Outline each uninfected red blood cell.
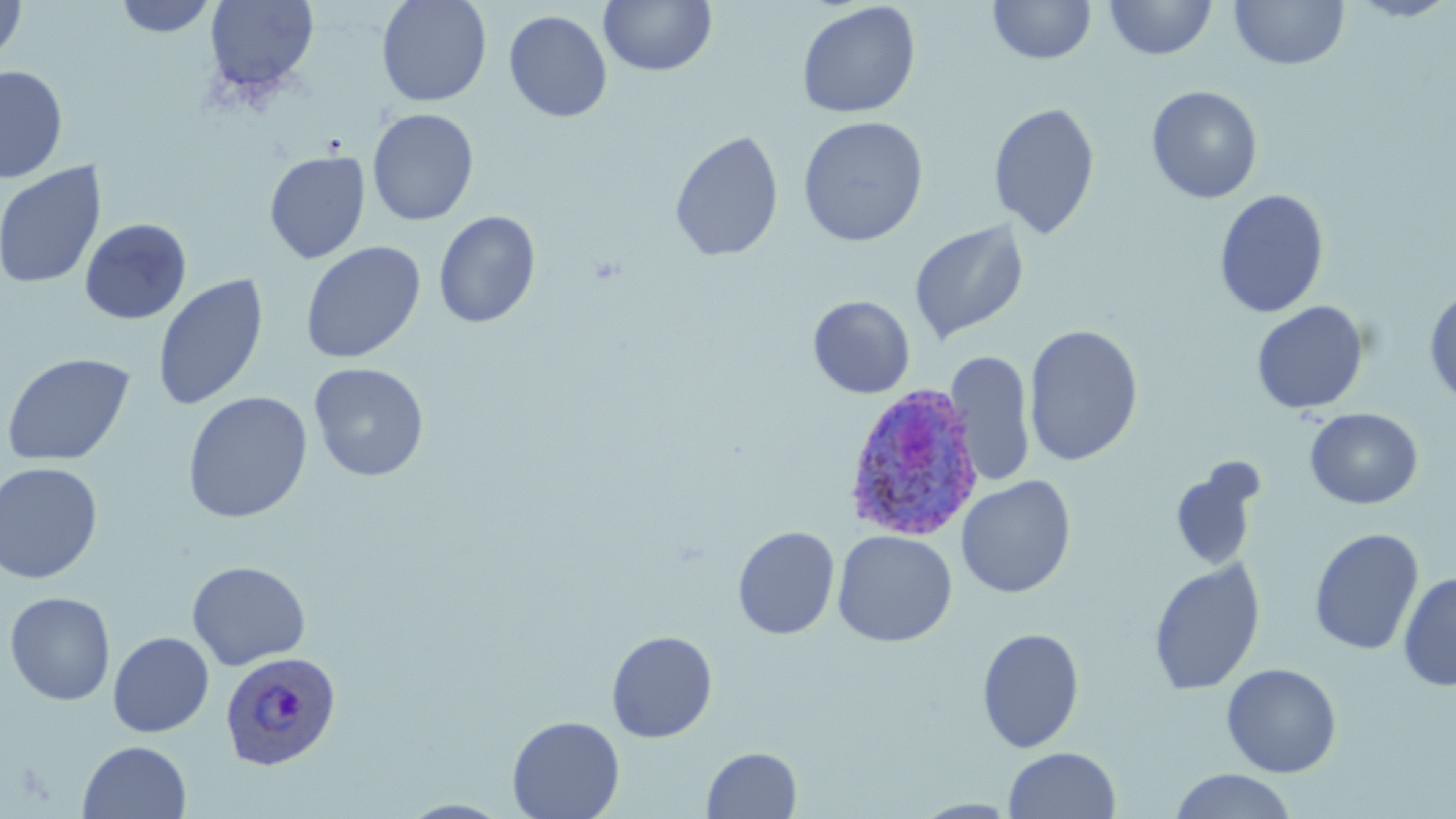

Approximate bounding boxes as (x1, y1, x2, y2) in pixels.
Uninfected red blood cells: (0, 0, 27, 65), (113, 0, 217, 37), (204, 0, 319, 95), (376, 0, 492, 107), (988, 0, 1096, 64), (1105, 0, 1217, 60), (1230, 0, 1349, 70), (1346, 0, 1456, 21), (599, 1, 717, 76), (796, 2, 921, 119), (503, 10, 613, 122), (0, 66, 67, 183), (1146, 85, 1263, 204), (988, 101, 1101, 239), (367, 108, 479, 226), (797, 116, 929, 247), (669, 130, 784, 262), (264, 150, 370, 264), (0, 161, 106, 290), (1214, 189, 1330, 318), (433, 210, 541, 328), (79, 218, 192, 324), (909, 219, 1029, 345), (300, 241, 426, 363), (152, 273, 268, 412), (1424, 284, 1456, 408), (808, 296, 915, 398), (1251, 300, 1369, 415), (1024, 324, 1144, 467), (946, 351, 1036, 488), (1, 352, 135, 467), (309, 362, 429, 481), (182, 391, 313, 523), (1304, 408, 1423, 509), (1169, 459, 1266, 572), (0, 461, 103, 584), (956, 475, 1076, 598), (733, 525, 840, 640), (1309, 527, 1424, 655), (832, 530, 957, 647), (1148, 557, 1266, 696), (186, 560, 311, 670), (1398, 572, 1456, 691), (4, 591, 115, 706), (977, 626, 1085, 753), (606, 630, 718, 743), (108, 631, 214, 737), (1221, 662, 1342, 777), (507, 715, 625, 819), (77, 740, 191, 819), (702, 746, 802, 819), (1003, 746, 1121, 818), (1169, 769, 1298, 819), (397, 799, 516, 818), (912, 799, 1022, 818).

Plasmodium ovale-infected red blood cell locations: (843, 382, 987, 542), (220, 650, 340, 771). Slide-level diagnosis: Plasmodium ovale. Thin blood smear. Light microscopy. Captured at 1000x magnification. May-Grünwald-Giemsa-stained preparation. Single field of view. Image is 1456×819 pixels.